Name the blood parasite species.
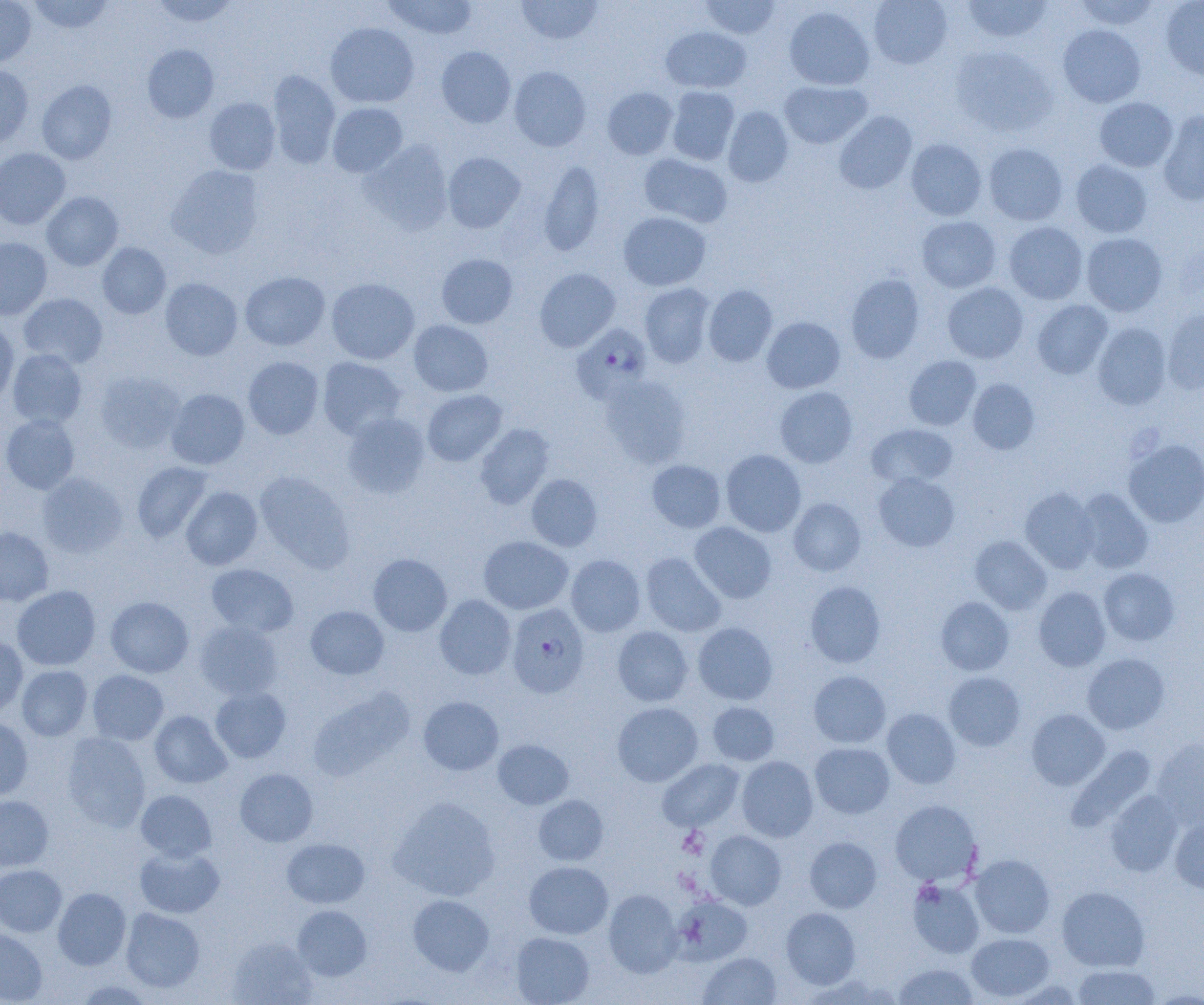

Plasmodium falciparum.

Summary:
  - Coordinate format: approximate bounding boxes as [x1, y1, x2, y2] in pixels
  - Platelet locations: [678, 827, 709, 858]
  - Plasmodium falciparum-infected red blood cell locations: [571, 323, 653, 403], [506, 603, 589, 698]
  - Uninfected red blood cell locations: [0, 0, 36, 67], [27, 0, 114, 35], [149, 0, 240, 27], [383, 0, 478, 40], [516, 0, 604, 45], [700, 0, 782, 40], [868, 0, 953, 69], [1073, 0, 1160, 31], [1160, 0, 1204, 82], [961, 1, 1052, 43], [784, 6, 875, 90], [325, 22, 419, 108], [1058, 24, 1146, 107], [660, 27, 751, 93], [142, 44, 219, 123], [436, 46, 516, 128], [950, 46, 1057, 138], [437, 57, 590, 136], [0, 66, 34, 148], [509, 66, 591, 151], [267, 70, 341, 168], [37, 79, 116, 164], [779, 80, 871, 149], [666, 86, 740, 165], [602, 87, 678, 159], [204, 97, 281, 174], [1094, 97, 1178, 172], [327, 102, 408, 177], [723, 106, 794, 187], [1157, 110, 1204, 205], [834, 111, 917, 194], [906, 139, 987, 220], [359, 140, 454, 235], [983, 143, 1068, 225], [0, 148, 70, 230], [442, 152, 525, 233], [638, 153, 732, 228], [538, 159, 605, 257], [1071, 159, 1153, 238], [166, 165, 264, 259], [41, 191, 123, 270], [618, 211, 711, 291], [916, 216, 1001, 292], [1003, 221, 1088, 304], [1081, 233, 1167, 316], [0, 238, 52, 319], [97, 243, 171, 319], [436, 253, 518, 328], [535, 268, 621, 352], [240, 271, 330, 351], [846, 274, 925, 363], [326, 277, 419, 364], [160, 278, 242, 360], [942, 282, 1028, 363], [639, 283, 716, 368], [703, 285, 778, 367], [19, 293, 108, 368], [1032, 300, 1113, 379], [1162, 309, 1204, 394], [761, 317, 845, 393], [0, 320, 19, 407], [409, 320, 493, 396], [1092, 323, 1172, 410], [7, 349, 87, 429], [904, 355, 982, 431], [243, 356, 324, 439], [317, 357, 406, 440], [95, 371, 185, 453], [599, 375, 692, 468], [967, 379, 1040, 454], [775, 386, 858, 468], [165, 389, 249, 469], [422, 389, 507, 467], [341, 412, 430, 499], [1, 414, 79, 494], [474, 423, 555, 509], [867, 424, 958, 488], [1123, 439, 1204, 527], [721, 449, 806, 537], [647, 460, 726, 532], [132, 461, 214, 542], [255, 471, 355, 572], [38, 472, 127, 557], [872, 473, 960, 552], [526, 474, 603, 551], [181, 486, 263, 570], [1019, 487, 1099, 573], [1075, 488, 1154, 574], [788, 497, 866, 576], [689, 522, 777, 603], [0, 527, 54, 606], [970, 535, 1052, 614], [478, 536, 573, 614], [640, 552, 725, 637], [368, 553, 452, 636], [566, 554, 646, 637], [207, 563, 298, 636], [1098, 568, 1180, 646], [805, 581, 886, 668], [12, 585, 100, 670], [1033, 587, 1111, 671], [434, 594, 516, 680], [105, 596, 194, 677], [935, 597, 1014, 675], [305, 605, 389, 680], [194, 621, 283, 700], [692, 622, 778, 705], [612, 626, 693, 706], [0, 637, 28, 718], [1082, 652, 1170, 734], [16, 665, 92, 740], [87, 669, 169, 745], [808, 670, 891, 748], [943, 671, 1025, 751], [210, 686, 291, 762], [418, 696, 504, 775], [612, 702, 703, 787], [707, 702, 779, 765], [882, 708, 961, 789], [1026, 709, 1110, 790], [150, 710, 232, 788], [0, 718, 33, 800], [62, 732, 151, 832], [1152, 738, 1204, 828], [493, 739, 573, 809], [810, 742, 894, 818], [1067, 745, 1156, 830], [736, 756, 818, 841], [657, 758, 744, 831], [235, 768, 318, 847], [1105, 789, 1183, 876], [136, 790, 216, 861], [0, 795, 53, 871], [533, 795, 608, 865], [389, 797, 500, 901], [889, 799, 982, 886], [1170, 816, 1204, 894], [705, 830, 786, 910], [804, 836, 882, 913], [281, 837, 370, 908], [134, 845, 225, 918], [970, 854, 1056, 939], [524, 861, 613, 939], [0, 864, 66, 937], [907, 879, 984, 958], [1057, 886, 1149, 971], [53, 887, 131, 970], [603, 889, 682, 977], [407, 894, 494, 975], [671, 894, 752, 965], [292, 905, 372, 981], [781, 907, 861, 989], [121, 908, 205, 992], [0, 928, 47, 1004], [510, 932, 594, 1005], [966, 932, 1054, 1001], [227, 936, 317, 1004], [697, 952, 781, 1005], [893, 963, 979, 1004], [1071, 963, 1161, 1004], [73, 979, 155, 1004]
  - Field of view: single
  - Magnification: 1000x
  - Modality: optical microscopy
  - Preparation: thin blood film
  - Image size: 1204×1005 pixels